State the blood parasite species.
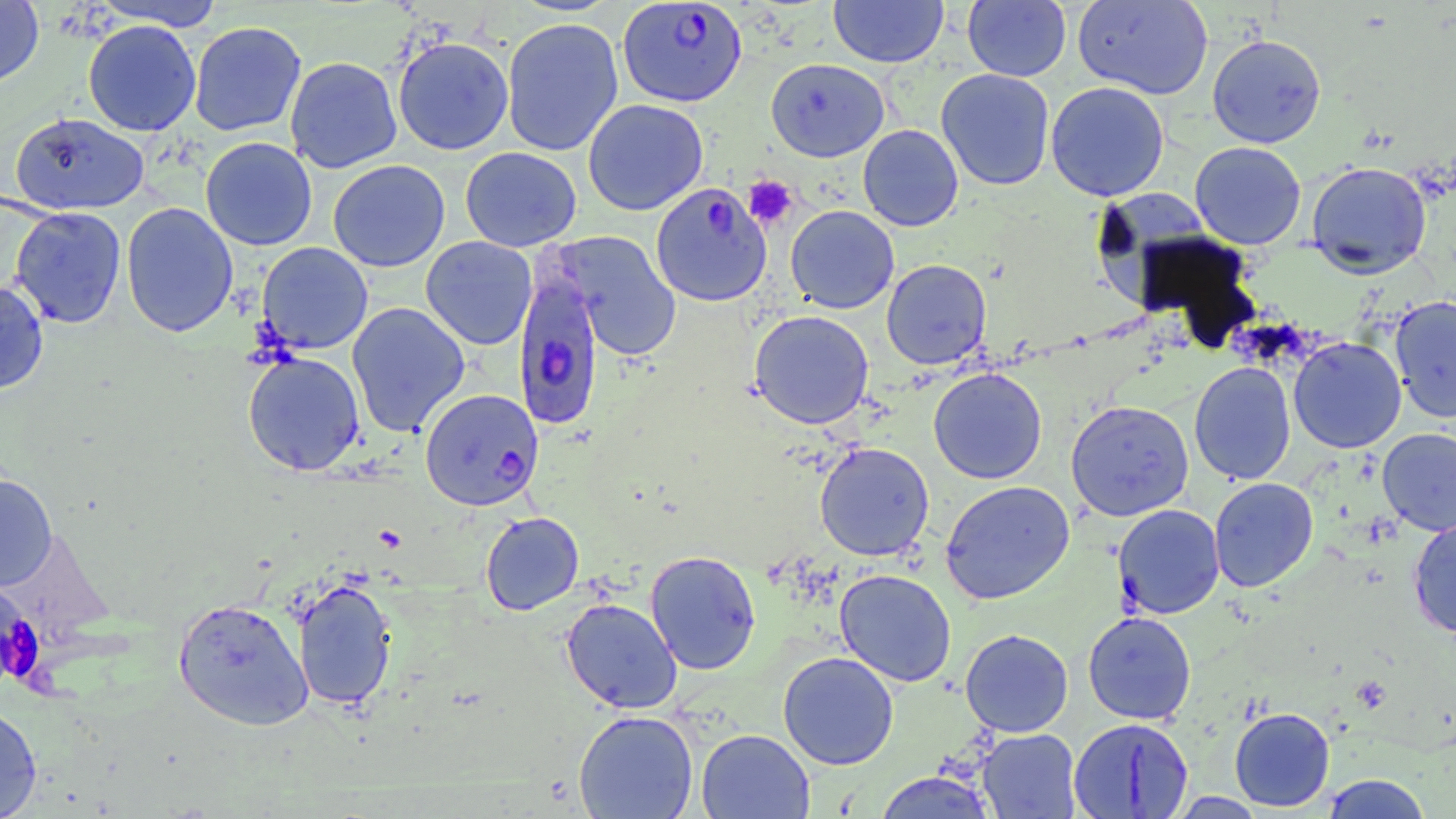

Plasmodium falciparum.

Approximate bounding boxes as (x1,y1)-(x2,y2) corner pairs in pixels. Plasmodium falciparum-infected red blood cell locations: (617,1)-(747,107), (513,267)-(606,431), (420,388)-(543,511). Uninfected red blood cell locations: (0,0)-(44,89), (92,0)-(225,31), (829,0)-(947,67), (963,0)-(1071,82), (1072,0)-(1214,99), (501,17)-(623,156), (83,19)-(201,137), (189,21)-(306,136), (1207,34)-(1326,148), (392,36)-(514,155), (285,56)-(402,173), (766,58)-(889,162), (936,69)-(1055,190), (1045,82)-(1169,201), (582,99)-(708,215), (9,111)-(150,215), (858,124)-(963,231), (200,136)-(317,251), (1189,141)-(1307,250), (460,146)-(581,252), (328,159)-(450,272), (1305,160)-(1432,277), (651,182)-(773,307), (1091,190)-(1222,310), (120,202)-(238,338), (786,205)-(899,314), (9,207)-(127,328), (553,231)-(682,361), (421,236)-(538,350), (257,242)-(373,354), (881,259)-(992,370), (0,280)-(49,393), (1389,295)-(1456,423), (346,302)-(470,437), (749,310)-(874,429), (1288,336)-(1406,453), (242,350)-(366,476), (1188,361)-(1296,485), (928,367)-(1047,484), (1065,399)-(1194,521), (1377,428)-(1456,536), (815,442)-(934,561), (0,473)-(58,590), (1209,477)-(1318,592), (940,480)-(1075,604), (1113,504)-(1225,619), (480,511)-(584,615), (1408,515)-(1456,639), (645,550)-(761,675), (834,569)-(957,687), (292,578)-(397,711), (561,597)-(683,713), (173,598)-(313,731), (1082,611)-(1196,725), (960,629)-(1073,737), (778,651)-(899,770), (0,703)-(42,819), (1229,706)-(1335,811), (573,710)-(699,819), (1068,717)-(1194,818), (696,729)-(814,819), (977,729)-(1081,818), (873,771)-(998,818), (1320,774)-(1434,818). Platelet locations: (744,176)-(798,229), (0,595)-(43,688). One field of a larger specimen. 1000x magnification. Thin blood smear. May-Grünwald-Giemsa-stained preparation. Optical microscopy. Image is 1456×819 pixels.